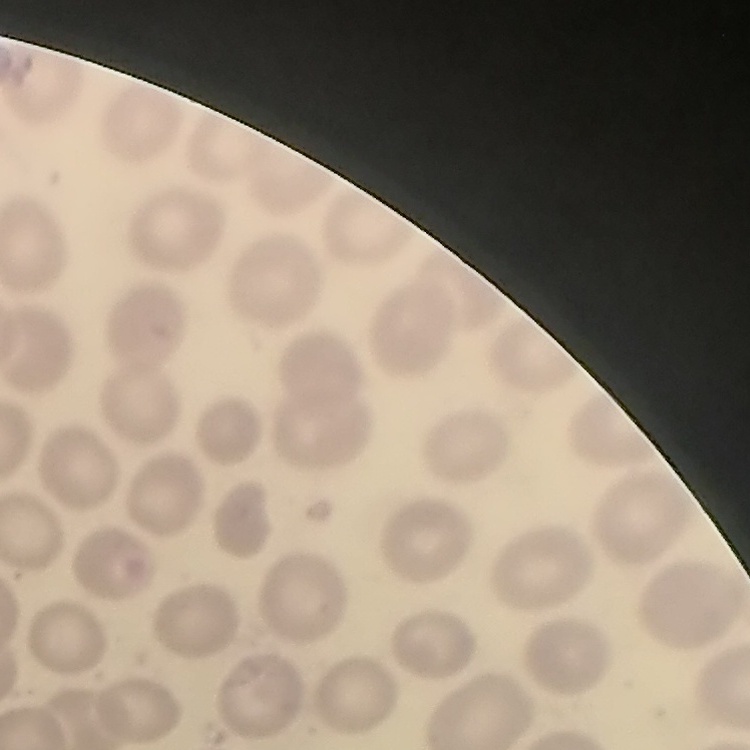
Summary:
  - Erythrocyte morphology: no rouleaux formation
  - Image type: square crop of a larger photomicrograph
  - Stain: Field's or Giemsa
  - Preparation: thin blood smear